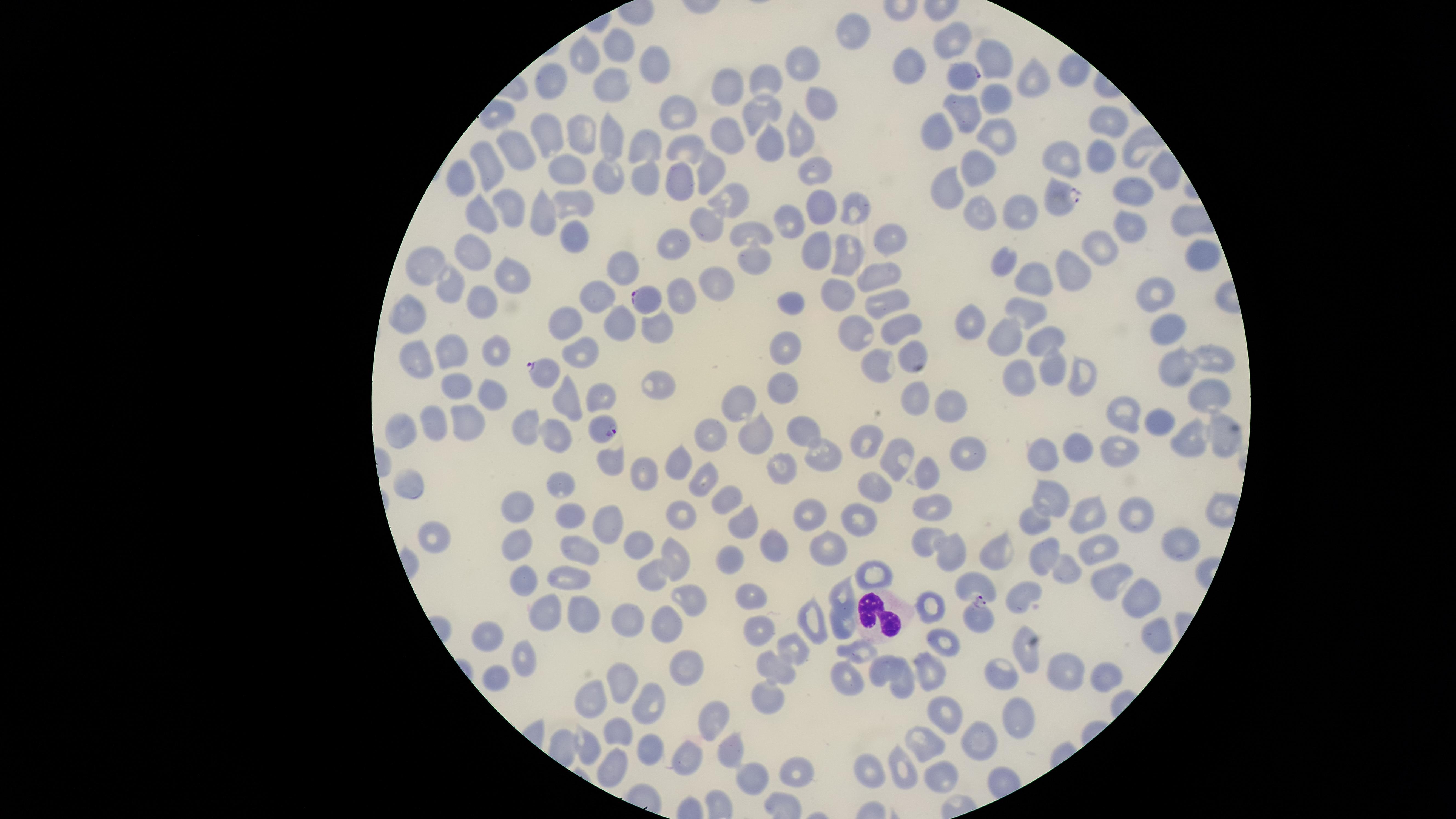
Approximate marker points as [x, y] in pixels. White blood cells: [881, 616]. Parasitized red blood cells: [967, 77], [1060, 197], [648, 297], [542, 372], [601, 427], [978, 616]. Uninfected red blood cells: [854, 34], [959, 43], [624, 45], [587, 49], [990, 60], [659, 62], [806, 62], [915, 68], [552, 76], [764, 76], [607, 78], [737, 80], [1037, 81], [989, 96], [817, 103], [968, 109], [760, 112], [680, 113], [1104, 121], [940, 126], [733, 131], [797, 131], [549, 132], [999, 133], [584, 140], [615, 141], [770, 143], [650, 145], [692, 145], [523, 146], [1100, 154], [1069, 160], [493, 167], [979, 167], [613, 171], [699, 173], [817, 173], [1161, 173], [464, 174], [571, 175], [646, 176], [680, 180], [949, 189], [1136, 194], [731, 195], [576, 201], [822, 203], [857, 205], [1024, 206], [515, 209], [984, 210], [488, 212], [545, 215], [790, 215], [704, 226], [1132, 226], [749, 232], [891, 234], [577, 235], [680, 243], [1106, 243], [819, 250], [851, 250], [474, 252], [429, 258], [753, 261], [1009, 264], [630, 268], [1073, 270], [512, 273], [878, 273], [1033, 278], [455, 283], [718, 284], [686, 290], [842, 292], [1151, 296], [890, 298], [598, 302], [793, 302], [483, 307], [1028, 309], [409, 316], [660, 324], [901, 324], [569, 326], [969, 327], [1165, 327], [621, 331], [857, 331], [1004, 337], [1038, 339], [455, 346], [584, 346], [494, 347], [786, 349], [909, 350], [415, 356], [1214, 357], [876, 365], [1049, 366], [1178, 366], [1014, 371], [1078, 372], [655, 383], [459, 385], [784, 388], [912, 389], [493, 394], [564, 395], [1208, 396], [600, 399], [742, 400], [946, 404], [1130, 411], [439, 419], [465, 424], [1164, 424], [528, 425], [711, 426], [400, 428], [556, 430], [803, 430], [1225, 430], [1188, 436], [763, 438], [866, 444], [1117, 445], [1082, 446], [823, 452], [1046, 453], [965, 456], [899, 458], [613, 460], [684, 466], [783, 467], [655, 472], [925, 476], [704, 478], [415, 483], [565, 484], [873, 488], [1053, 496], [728, 498], [518, 507], [934, 508], [680, 510], [1136, 510], [572, 511], [1092, 512], [812, 516], [1036, 516], [745, 523], [858, 523], [605, 524], [439, 538], [925, 538], [1179, 540], [516, 542], [641, 542], [831, 542], [774, 545], [1101, 546], [582, 553], [995, 553], [1034, 554], [732, 556], [952, 556], [675, 557], [1067, 569], [652, 570], [570, 572], [871, 574], [520, 579], [1112, 580], [977, 582], [1027, 592], [687, 595], [843, 595], [749, 596], [1136, 597], [542, 603], [933, 605], [583, 611], [626, 617], [847, 623], [669, 626], [811, 626], [758, 629], [491, 636], [1151, 637], [950, 642], [796, 647], [859, 652], [1028, 652], [528, 659], [691, 661], [930, 663], [779, 667], [1002, 667], [879, 670], [1063, 671], [496, 675], [906, 675], [1108, 675], [627, 677], [845, 682], [764, 692], [597, 693], [647, 700], [1021, 708], [946, 718], [617, 726], [709, 731], [983, 734], [930, 744], [586, 745], [652, 749], [734, 749], [690, 763], [871, 766], [612, 767], [901, 767], [796, 773], [754, 777], [939, 778]. Image is 1456×819 pixels. Photographed with a smartphone camera through the microscope eyepiece. One field of view of the specimen. Giemsa-stained preparation. Thin blood film. Species: Plasmodium falciparum. Circular visible region. Presence: malaria parasites identified.